Identify the parasite.
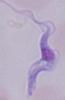
This is a trypanosome.

Captured at 1000x magnification. Photomicrograph.